Comment on the morphology of the red blood cells.
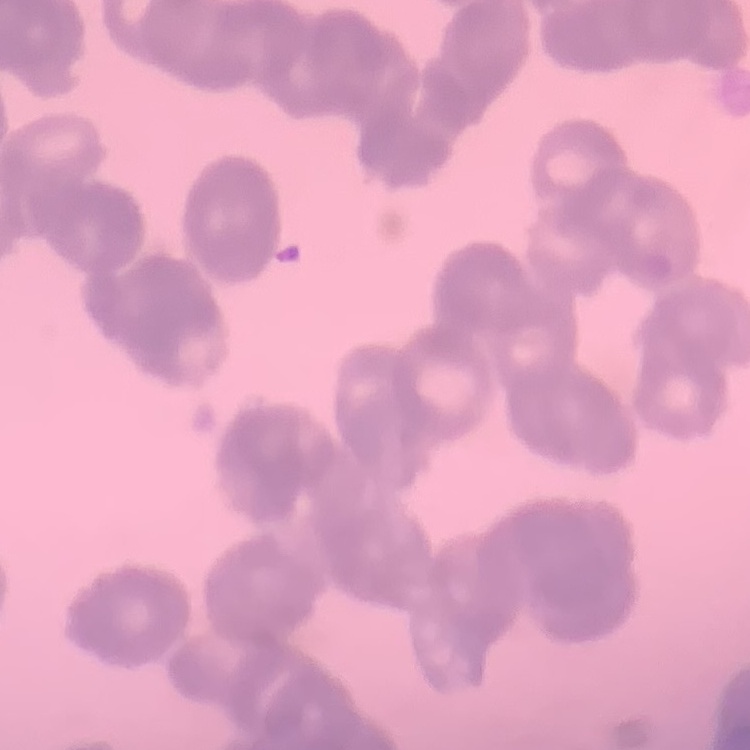
They show rouleaux formation.

Stained with either Field's or Giemsa. Thin blood smear. One tile cut from a larger photomicrograph.